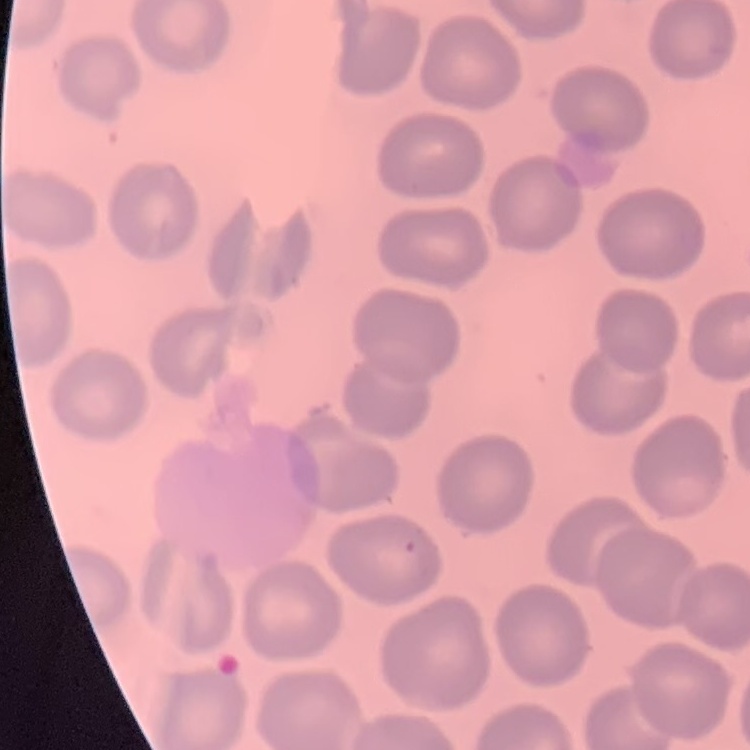
Summary:
  - Red blood cell morphology: no rouleaux formation
  - Image type: square crop of a larger photomicrograph
  - Preparation: thin blood film
  - Stain: Field's or Giemsa